Identify the parasite.
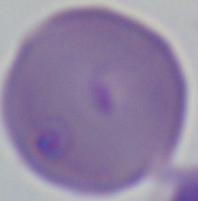
Babesia.

Photomicrograph. 1000x magnification.